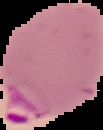

Summary:
  - Preparation: thin blood smear
  - Malaria status: parasitized
  - Image size: 103×130 pixels
  - Image type: segmented cell region with the area outside set to black